Identify the parasite.
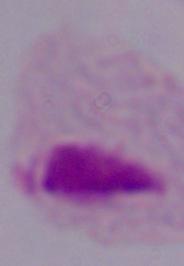

This is a trichomonad.

{
  "magnification": "1000x",
  "modality": "photomicrograph"
}